Classify this cell by malaria status.
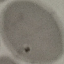

It is uninfected.

capture: smartphone through the microscope eyepiece
image_type: cell patch, automatically extracted from a larger field of view and resized to 64 × 64 pixels
preparation: thin blood film
stain: Giemsa